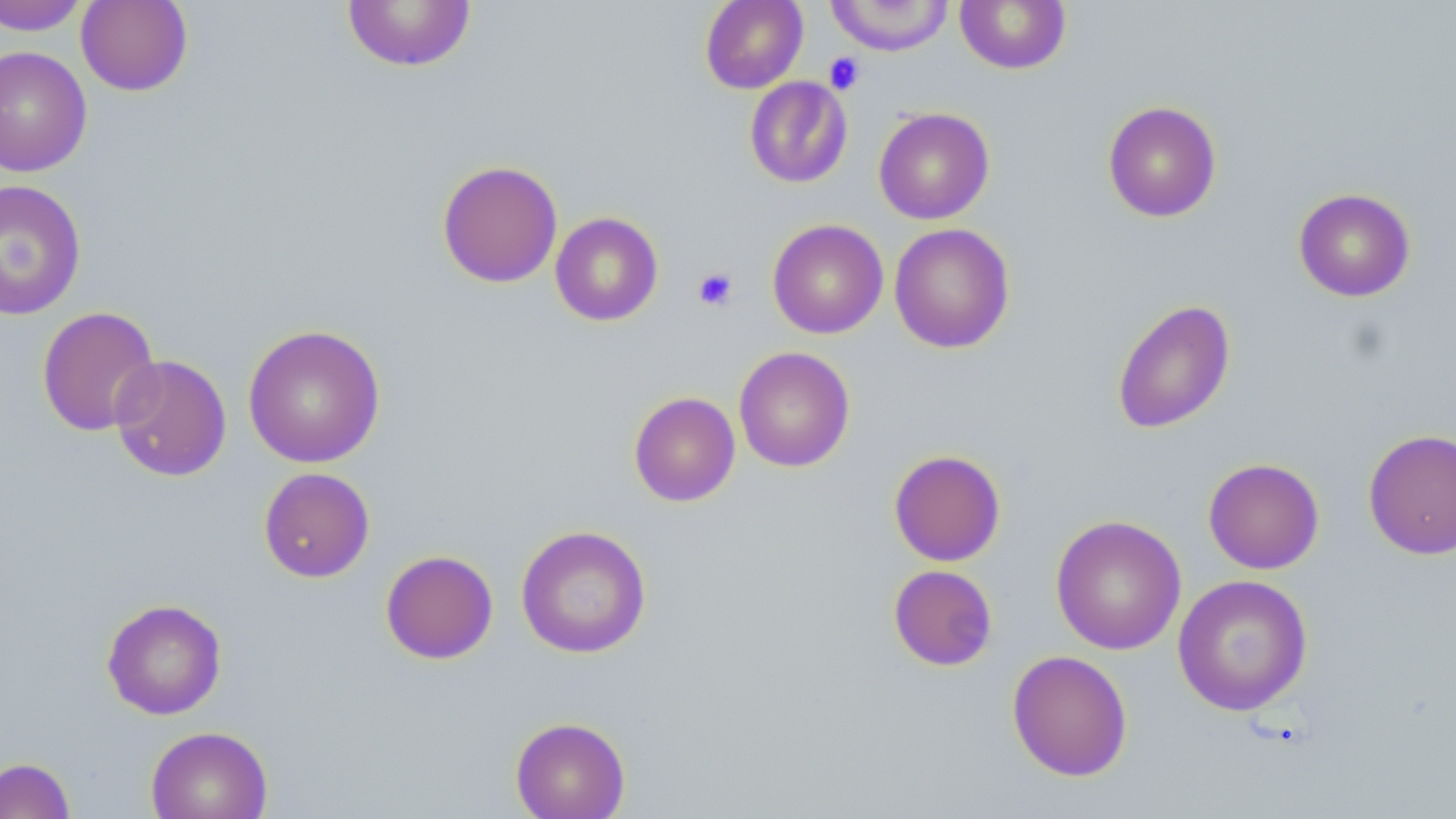
slide-level diagnosis = negative for blood parasites
field of view = one of a larger specimen
platelet locations = approximate bounding boxes as (x1,y1)-(x2,y2) corner pairs in pixels: (824,51)-(865,94), (693,266)-(738,311)
modality = optical microscopy
image size = 1456×819 pixels
stain = May-Grünwald-Giemsa
magnification = 1000x
uninfected red blood cell locations = approximate bounding boxes as (x1,y1)-(x2,y2) corner pairs in pixels: (76,0)-(193,96), (699,0)-(808,93), (827,0)-(954,56), (955,0)-(1072,74), (0,1)-(91,35), (342,1)-(477,72), (0,46)-(92,177), (744,76)-(853,188), (1102,100)-(1222,223), (873,107)-(995,224), (436,159)-(563,288), (0,178)-(87,320), (1293,188)-(1416,302), (550,212)-(664,326), (767,219)-(889,339), (889,223)-(1015,353), (1111,299)-(1236,434), (36,306)-(161,437), (242,324)-(386,468), (733,346)-(855,473), (109,353)-(232,482), (628,391)-(740,507), (1363,428)-(1456,561), (888,449)-(1006,567), (1203,458)-(1325,574), (258,467)-(375,583), (1050,514)-(1186,655), (516,524)-(651,659), (380,549)-(499,664), (887,564)-(998,671), (1172,573)-(1313,716), (101,598)-(227,720), (1007,649)-(1133,781), (509,716)-(631,819), (145,725)-(273,819), (0,757)-(76,819)
preparation = thin blood film